Identify the parasite.
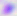
This is Toxoplasma gondii.

Summary:
  - Modality: micrograph
  - Magnification: 400x